Assess the morphology of the red blood cells.
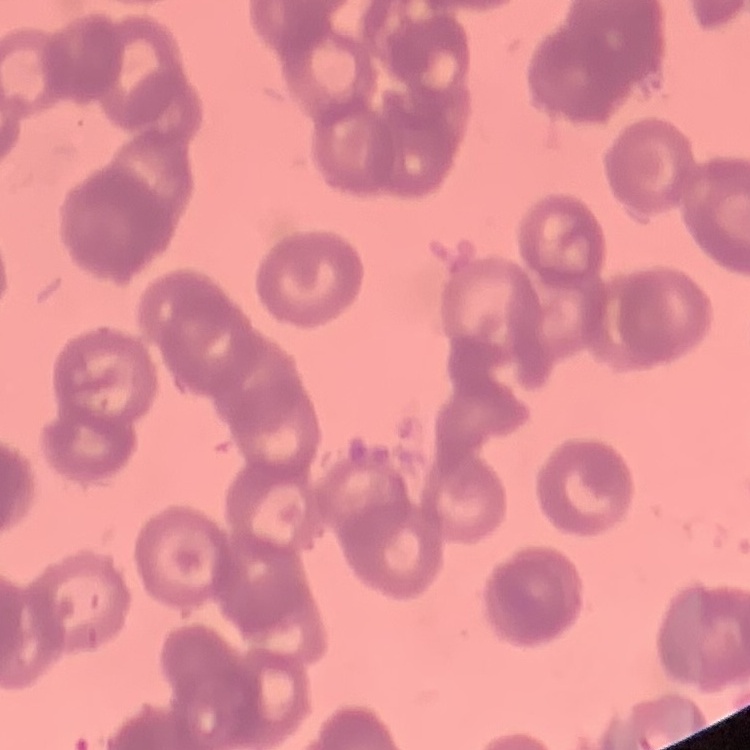

Rouleaux formation.

Thin peripheral smear. Square crop of a larger photomicrograph. Stained with either Field's or Giemsa.